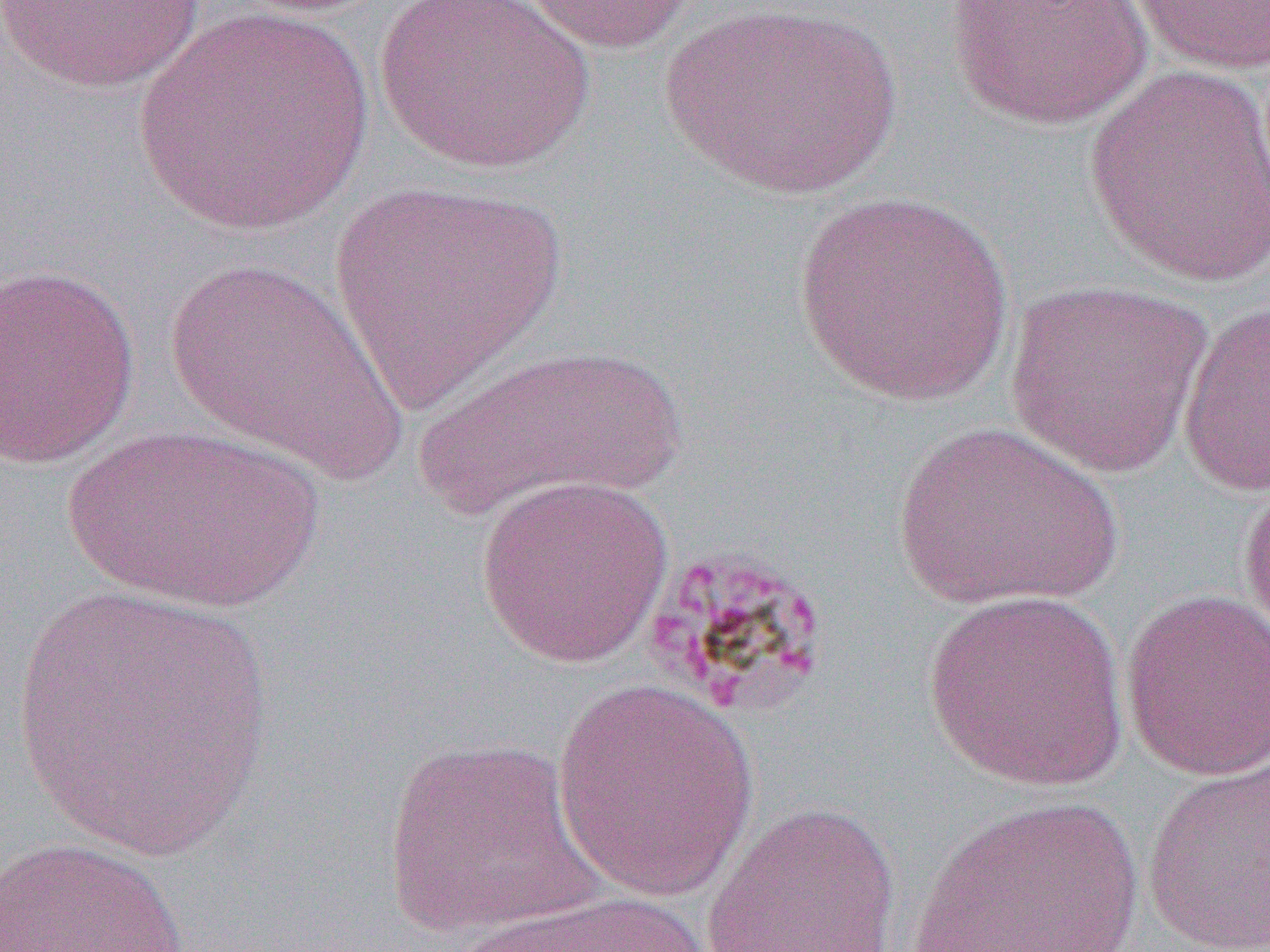
Approximate bounding boxes as (x1,y1)-(x2,y2) corner pairs in pixels. Uninfected red blood cell locations: (373,0)-(596,175), (513,0)-(701,55), (944,0)-(1154,132), (1126,0)-(1269,76), (0,2)-(211,95), (655,3)-(907,202), (132,4)-(373,238), (1084,61)-(1270,289), (328,179)-(567,419), (793,190)-(1016,409), (162,255)-(410,486), (0,262)-(141,469), (1004,278)-(1215,479), (1177,298)-(1270,497), (411,341)-(688,524), (890,421)-(1124,615), (59,423)-(325,613), (1237,472)-(1270,653), (473,473)-(675,669), (1,582)-(277,863), (1119,588)-(1270,783), (921,589)-(1132,793), (551,679)-(762,902), (381,736)-(602,939), (1141,759)-(1270,952), (910,795)-(1148,952), (701,801)-(902,951), (0,836)-(191,951), (447,890)-(714,952). Slide-level diagnosis: Plasmodium malariae. Captured at 1000x magnification. One field of a larger specimen. Image is 1270×952 pixels. Light microscopy. Thin blood film.